State which parasite is depicted.
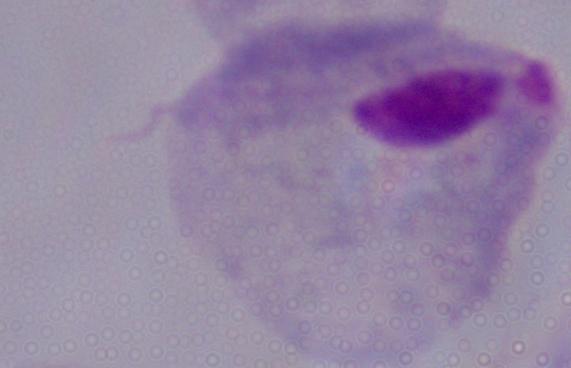
This is a trichomonad.

Photomicrograph. Captured at 1000x magnification.